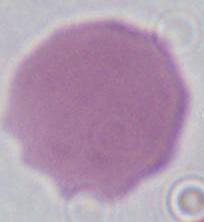
Summary:
  - Identification: red blood cell
  - Magnification: 1000x
  - Modality: photomicrograph